Assess this cell for malaria.
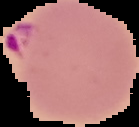

Parasitized.

preparation = thin blood smear
image type = segmented cell region with the area outside set to black
image size = 139×127 pixels